State which parasite is depicted.
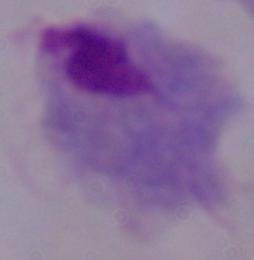

This is a trichomonad.

Summary:
  - Magnification: 1000x
  - Modality: micrograph